Name the blood parasite species.
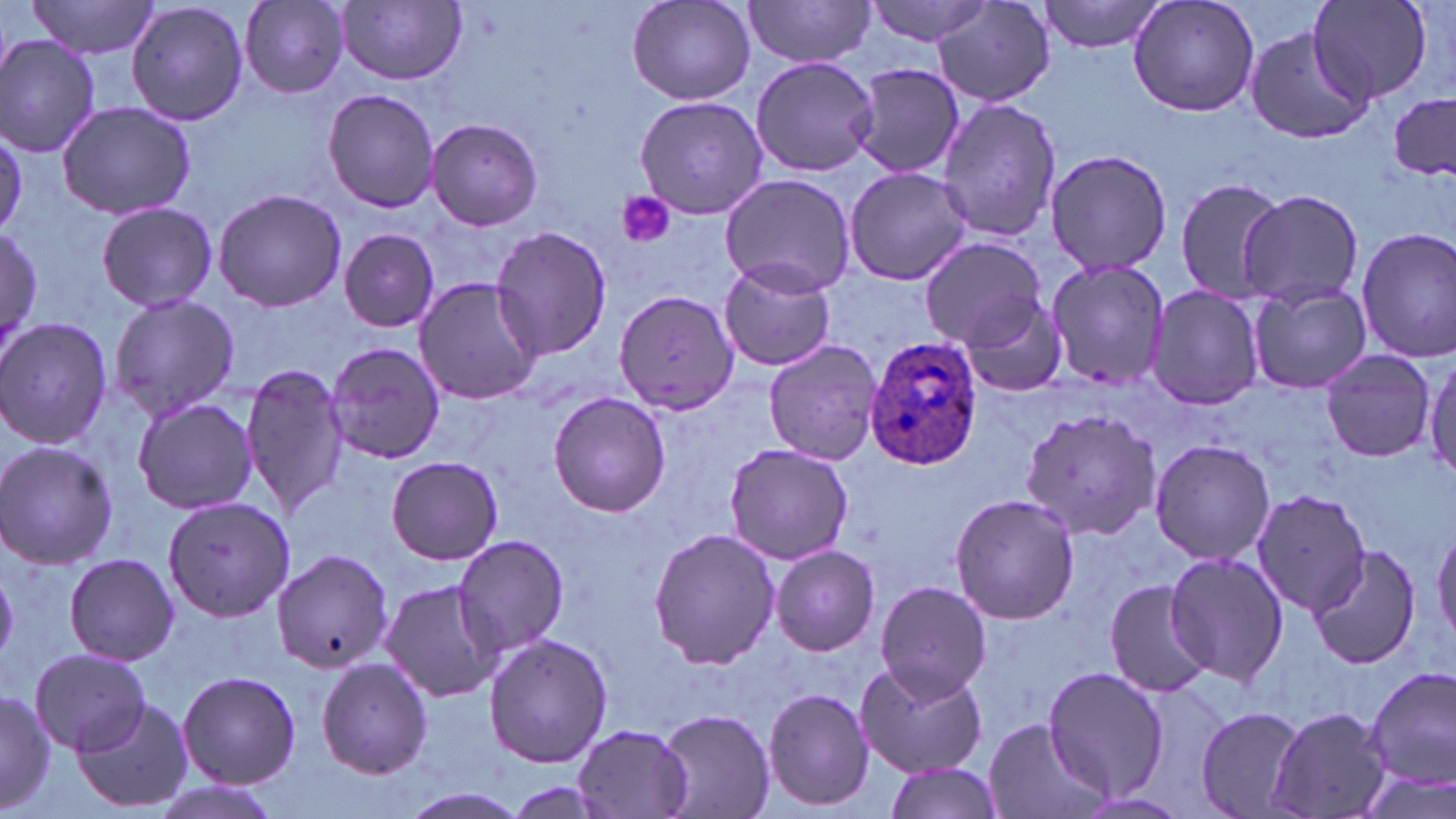
Plasmodium ovale.

Approximate bounding boxes as named x1/y1/x2/y2 corners in pixels. Plasmodium ovale-infected red blood cell locations: (x1=865, y1=337, x2=984, y2=470). Platelet locations: (x1=615, y1=192, x2=677, y2=249). Uninfected red blood cell locations: (x1=27, y1=0, x2=161, y2=59), (x1=626, y1=0, x2=757, y2=107), (x1=865, y1=0, x2=995, y2=47), (x1=1038, y1=0, x2=1169, y2=54), (x1=1129, y1=0, x2=1259, y2=118), (x1=1308, y1=0, x2=1434, y2=104), (x1=125, y1=1, x2=252, y2=128), (x1=239, y1=1, x2=351, y2=97), (x1=743, y1=1, x2=877, y2=68), (x1=339, y1=2, x2=468, y2=85), (x1=933, y1=2, x2=1056, y2=108), (x1=1242, y1=25, x2=1372, y2=145), (x1=0, y1=34, x2=101, y2=158), (x1=750, y1=57, x2=879, y2=176), (x1=847, y1=61, x2=967, y2=179), (x1=321, y1=89, x2=442, y2=213), (x1=1388, y1=94, x2=1456, y2=180), (x1=634, y1=95, x2=767, y2=219), (x1=935, y1=97, x2=1061, y2=244), (x1=56, y1=100, x2=196, y2=221), (x1=425, y1=118, x2=544, y2=231), (x1=1045, y1=148, x2=1172, y2=277), (x1=840, y1=168, x2=974, y2=287), (x1=719, y1=173, x2=855, y2=296), (x1=1172, y1=177, x2=1287, y2=303), (x1=213, y1=187, x2=346, y2=313), (x1=1236, y1=188, x2=1363, y2=309), (x1=95, y1=201, x2=218, y2=312), (x1=489, y1=226, x2=614, y2=361), (x1=1, y1=227, x2=44, y2=353), (x1=1355, y1=227, x2=1456, y2=362), (x1=338, y1=229, x2=440, y2=333), (x1=917, y1=236, x2=1045, y2=349), (x1=717, y1=257, x2=839, y2=373), (x1=1045, y1=257, x2=1171, y2=390), (x1=412, y1=276, x2=544, y2=405), (x1=1246, y1=281, x2=1374, y2=394), (x1=1146, y1=283, x2=1266, y2=411), (x1=614, y1=289, x2=739, y2=415), (x1=107, y1=290, x2=240, y2=422), (x1=960, y1=294, x2=1066, y2=398), (x1=0, y1=317, x2=115, y2=448), (x1=762, y1=337, x2=884, y2=465), (x1=327, y1=341, x2=444, y2=464), (x1=1317, y1=348, x2=1437, y2=462), (x1=1425, y1=351, x2=1456, y2=483), (x1=240, y1=362, x2=350, y2=519), (x1=548, y1=393, x2=670, y2=516), (x1=132, y1=396, x2=261, y2=516), (x1=1017, y1=404, x2=1162, y2=543), (x1=1148, y1=438, x2=1276, y2=566), (x1=0, y1=441, x2=119, y2=570), (x1=723, y1=442, x2=854, y2=565), (x1=387, y1=456, x2=503, y2=564), (x1=1248, y1=488, x2=1371, y2=614), (x1=948, y1=492, x2=1079, y2=627), (x1=162, y1=496, x2=295, y2=622), (x1=1431, y1=519, x2=1456, y2=648), (x1=646, y1=527, x2=780, y2=671), (x1=451, y1=532, x2=570, y2=657), (x1=1302, y1=539, x2=1421, y2=668), (x1=770, y1=544, x2=881, y2=657), (x1=271, y1=548, x2=392, y2=675), (x1=1162, y1=551, x2=1289, y2=687), (x1=61, y1=552, x2=181, y2=666), (x1=379, y1=578, x2=505, y2=703), (x1=1102, y1=578, x2=1216, y2=699), (x1=876, y1=581, x2=992, y2=700), (x1=483, y1=634, x2=613, y2=769), (x1=31, y1=651, x2=152, y2=753), (x1=316, y1=657, x2=433, y2=779), (x1=855, y1=662, x2=987, y2=777), (x1=1367, y1=664, x2=1456, y2=792), (x1=1042, y1=667, x2=1170, y2=802), (x1=177, y1=669, x2=300, y2=789), (x1=0, y1=685, x2=53, y2=813), (x1=762, y1=686, x2=876, y2=814), (x1=71, y1=694, x2=194, y2=813), (x1=1193, y1=705, x2=1310, y2=819), (x1=1267, y1=705, x2=1393, y2=819), (x1=655, y1=706, x2=774, y2=818), (x1=983, y1=717, x2=1110, y2=819), (x1=572, y1=724, x2=695, y2=819), (x1=882, y1=761, x2=1003, y2=819), (x1=1349, y1=765, x2=1454, y2=819), (x1=392, y1=787, x2=535, y2=819). 1000x magnification. May-Grünwald-Giemsa stain. Image is 1456×819 pixels. Thin blood smear. Single field of view. Optical microscopy.